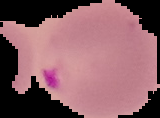
From a thin blood film. Image is 160×118 pixels. Result: malaria parasites identified. The area outside the segmented cell region is set to black.